Classify this cell by malaria status.
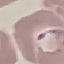

It is parasitized.

Summary:
  - Preparation: thin blood smear
  - Capture: smartphone through the microscope eyepiece
  - Image type: automatically extracted cell patch, resized to 64 × 64 pixels
  - Stain: Giemsa